Identify the parasite.
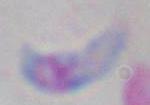

Toxoplasma gondii.

Summary:
  - Magnification: 1000x
  - Modality: photomicrograph